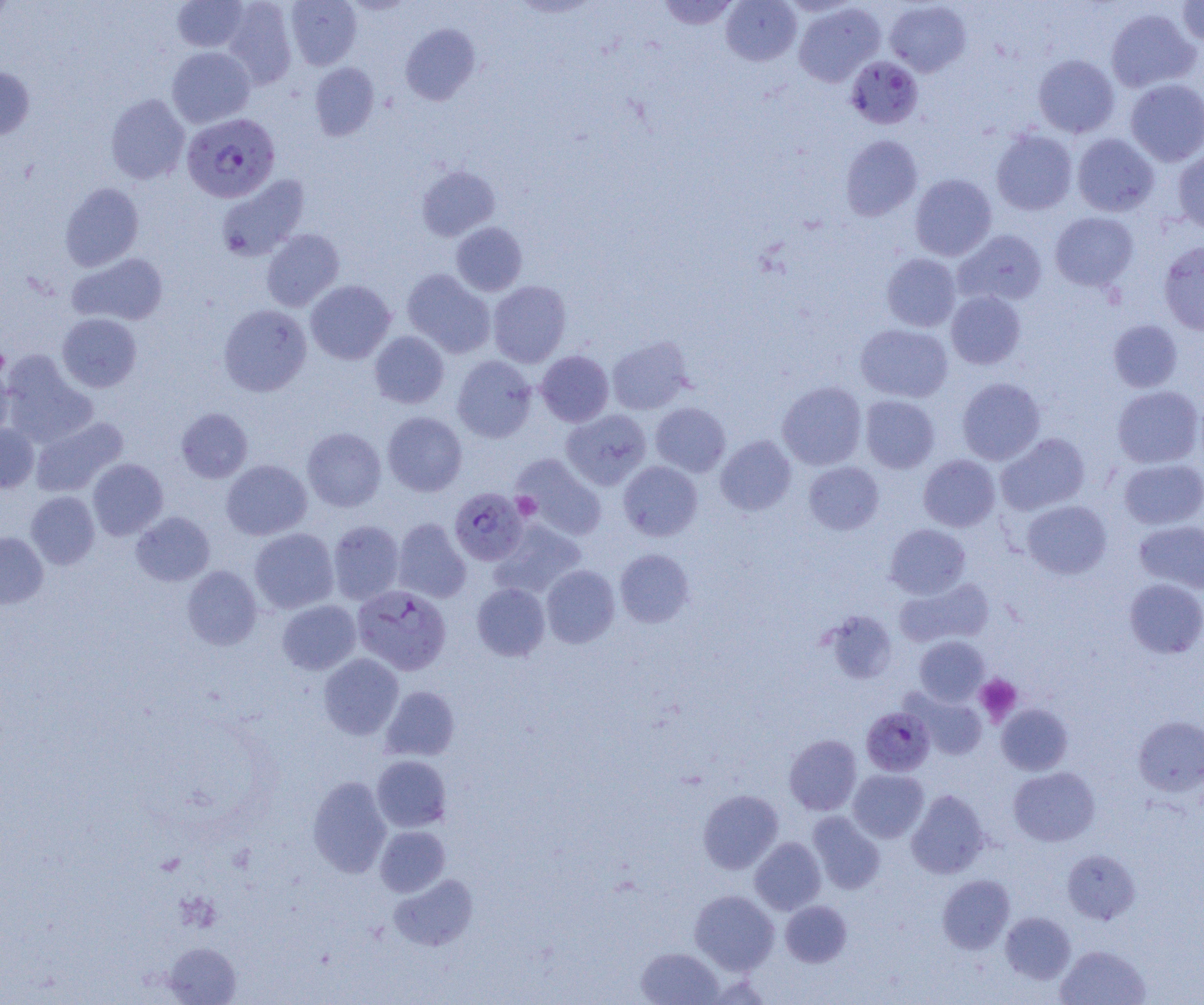
Approximate bounding boxes as (x1, y1, x2, y2) in pixels. Uninfected red blood cell locations: (172, 0, 249, 52), (222, 0, 297, 88), (286, 0, 362, 69), (658, 0, 739, 30), (721, 0, 802, 66), (1177, 0, 1204, 46), (339, 1, 418, 15), (885, 1, 971, 76), (794, 4, 884, 87), (1105, 8, 1201, 93), (401, 23, 480, 105), (167, 47, 255, 127), (1033, 54, 1119, 138), (309, 62, 379, 141), (0, 66, 34, 140), (1125, 79, 1204, 166), (105, 94, 190, 184), (991, 129, 1078, 215), (1072, 133, 1159, 217), (840, 135, 922, 220), (1172, 148, 1204, 233), (416, 165, 500, 241), (910, 174, 997, 261), (216, 175, 310, 262), (60, 183, 144, 271), (1050, 212, 1138, 291), (451, 222, 527, 296), (261, 229, 344, 311), (954, 229, 1047, 306), (1159, 241, 1204, 335), (68, 252, 168, 326), (881, 253, 961, 332), (402, 269, 495, 357), (306, 280, 395, 364), (488, 280, 571, 367), (946, 291, 1026, 369), (219, 304, 311, 396), (57, 313, 142, 392), (1108, 319, 1182, 392), (855, 323, 953, 402), (369, 331, 449, 408), (607, 336, 692, 415), (536, 350, 614, 426), (1, 353, 98, 447), (452, 356, 537, 443), (0, 362, 14, 442), (957, 377, 1045, 465), (777, 382, 867, 470), (1111, 385, 1203, 468), (860, 395, 939, 473), (650, 402, 730, 476), (176, 408, 253, 483), (561, 409, 652, 490), (382, 411, 468, 496), (31, 417, 127, 496), (0, 424, 39, 492), (303, 427, 386, 511), (997, 433, 1090, 515), (715, 435, 796, 516), (918, 452, 1089, 527), (512, 454, 607, 541), (919, 454, 1000, 531), (87, 458, 168, 540), (1119, 458, 1204, 529), (222, 459, 312, 540), (619, 461, 702, 541), (804, 462, 884, 535), (26, 491, 100, 568), (1021, 500, 1112, 580), (131, 511, 214, 586), (393, 518, 471, 603), (490, 519, 586, 598), (1134, 519, 1204, 594), (328, 520, 404, 604), (885, 524, 970, 599), (249, 528, 338, 613), (0, 531, 48, 608), (615, 548, 695, 627), (181, 565, 262, 650), (541, 565, 620, 647), (895, 577, 994, 647), (1124, 578, 1204, 658), (472, 582, 550, 661), (277, 600, 360, 675), (823, 610, 898, 684), (914, 636, 990, 706), (319, 653, 403, 739), (380, 685, 460, 761), (909, 691, 987, 760), (996, 703, 1073, 775), (1134, 715, 1204, 796), (784, 734, 862, 815), (372, 755, 451, 832), (1009, 767, 1100, 846), (847, 769, 929, 842), (307, 775, 391, 877), (698, 789, 784, 874), (907, 789, 990, 879), (808, 812, 886, 894), (376, 826, 450, 897), (750, 837, 826, 914), (1063, 849, 1140, 924), (389, 874, 478, 950), (938, 874, 1014, 954), (689, 890, 779, 974), (780, 900, 852, 967), (1001, 911, 1075, 984), (163, 942, 241, 1004), (1055, 944, 1150, 1005), (636, 947, 723, 1005). Plasmodium falciparum-infected red blood cell locations: (845, 56, 923, 129), (182, 113, 280, 202), (449, 487, 528, 565), (352, 585, 451, 675), (861, 707, 935, 776). Platelet locations: (0, 342, 9, 380), (512, 493, 540, 519), (975, 674, 1022, 725). Slide-level diagnosis: Plasmodium falciparum. Captured at 1000x magnification. Light microscopy. Image is 1204×1005 pixels. Single field of view. Thin blood smear.